Identify the parasite.
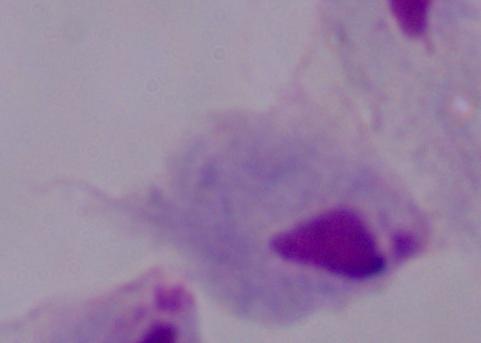

A trichomonad.

Micrograph. 1000x magnification.